Locate every leukocyte (white blood cell).
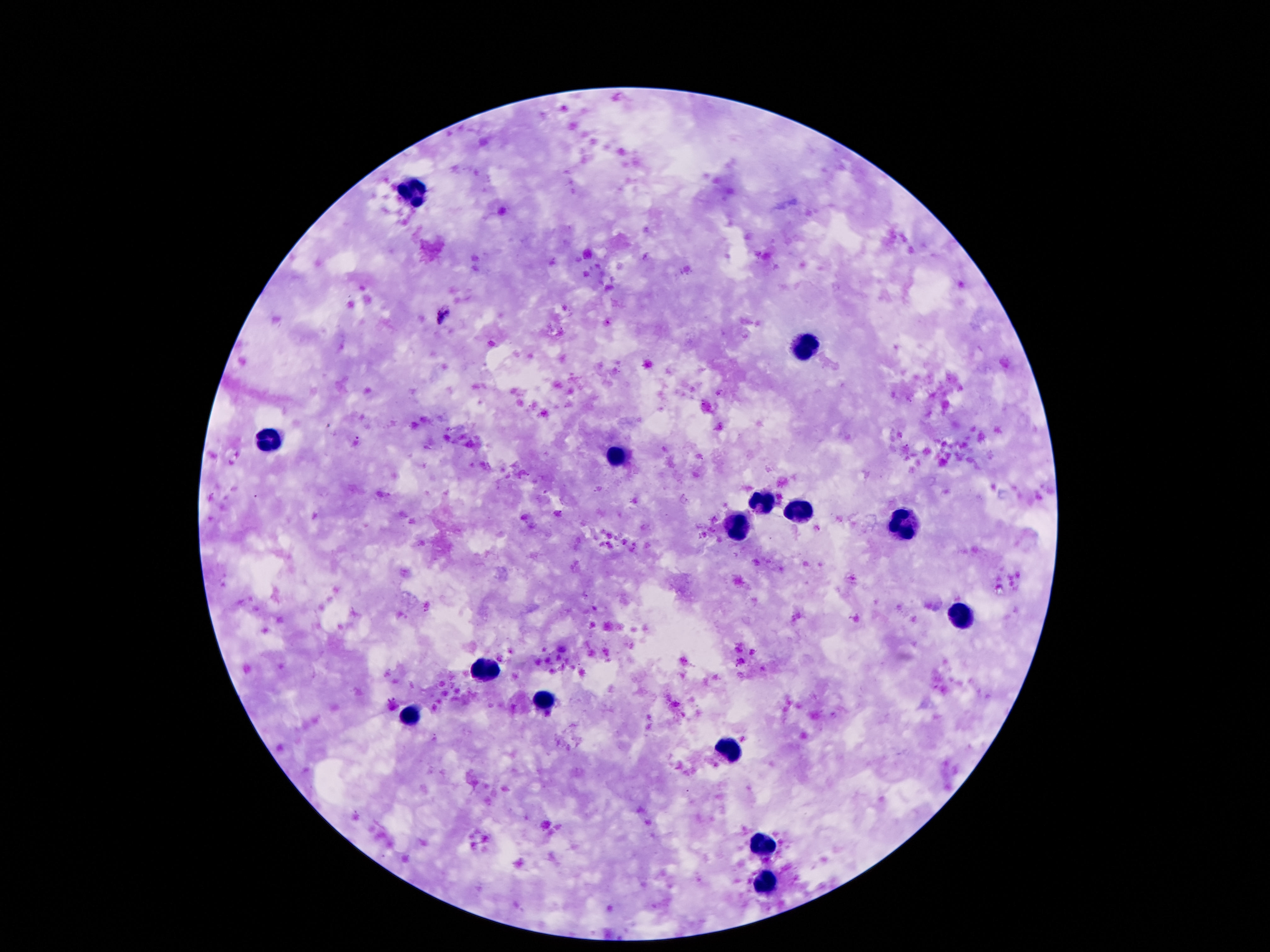

Approximate centers as (x, y) in pixels.
Leukocytes: (410, 195), (808, 344), (269, 439), (617, 458), (759, 501), (804, 512), (902, 523), (738, 525), (957, 613), (480, 664), (539, 699), (406, 719), (726, 749), (765, 841), (765, 888).

magnification = 100x
image size = 1270×952 pixels
capture = smartphone camera through the microscope eyepiece
field of view = one from this slide
stain = Giemsa
preparation = thick blood smear
patient malaria status = uninfected